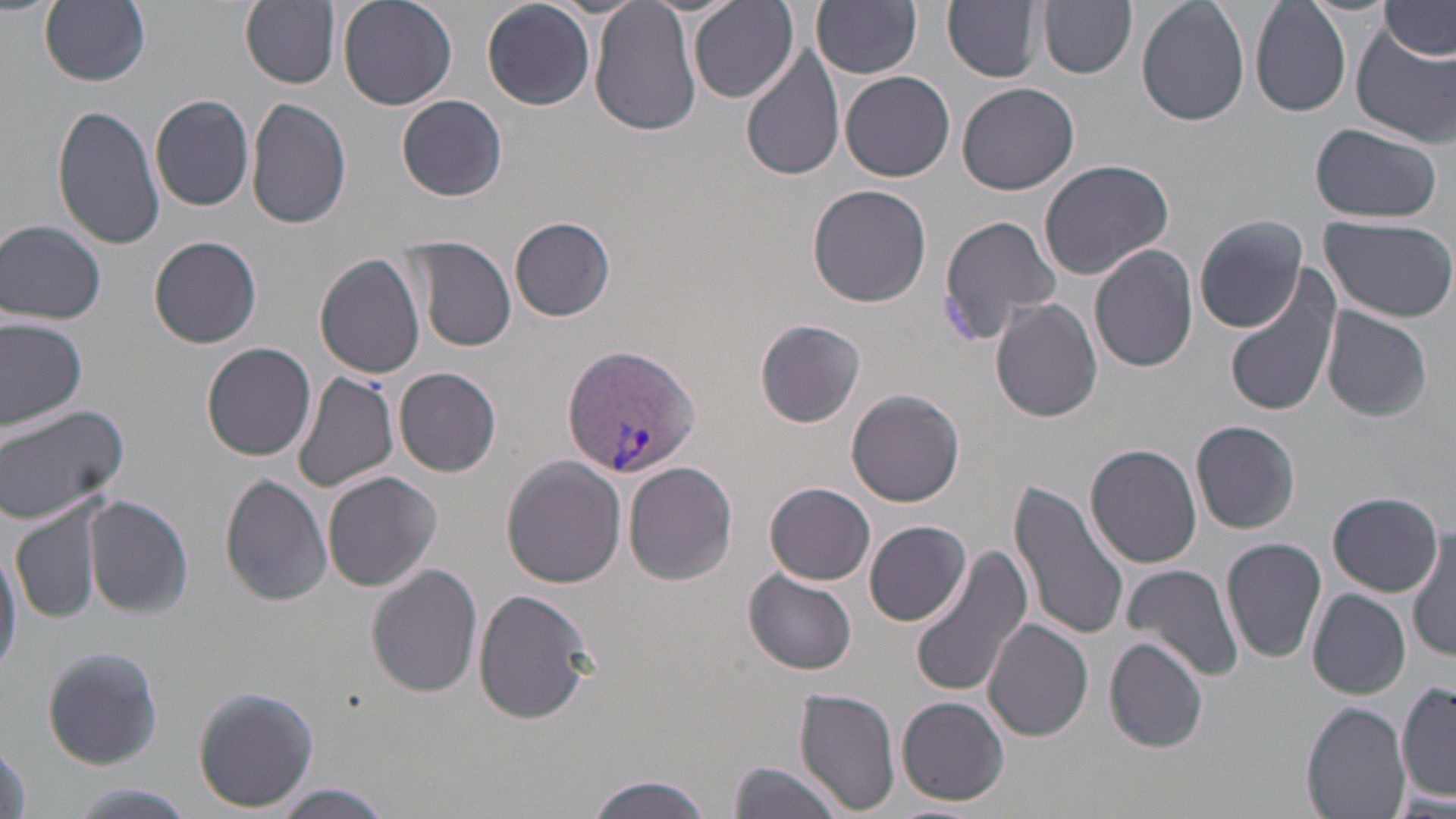

Summary:
  - Coordinate format: approximate bounding boxes as (x1, y1, x2, y2) in pixels
  - Plasmodium vivax-infected red blood cell locations: (563, 344, 700, 477)
  - Uninfected red blood cell locations: (237, 0, 342, 89), (337, 0, 457, 112), (944, 0, 1045, 83), (1040, 0, 1137, 78), (1137, 0, 1251, 126), (1378, 0, 1455, 61), (40, 1, 151, 88), (482, 1, 596, 110), (589, 1, 702, 137), (812, 1, 922, 77), (1250, 1, 1354, 118), (689, 2, 799, 104), (1352, 24, 1455, 146), (739, 46, 847, 180), (841, 71, 955, 181), (958, 82, 1079, 196), (397, 94, 509, 201), (151, 96, 255, 212), (245, 98, 352, 230), (52, 102, 167, 252), (1310, 123, 1443, 224), (1038, 157, 1174, 282), (808, 184, 932, 307), (940, 214, 1062, 342), (1194, 215, 1309, 332), (510, 216, 615, 321), (1320, 216, 1456, 324), (1, 219, 107, 325), (150, 236, 262, 347), (412, 238, 516, 351), (1089, 244, 1197, 373), (314, 253, 427, 379), (1224, 268, 1342, 419), (990, 298, 1103, 422), (1321, 305, 1433, 422), (0, 316, 88, 430), (759, 319, 867, 425), (201, 343, 318, 460), (393, 367, 503, 475), (292, 370, 401, 495), (848, 388, 964, 506), (0, 404, 129, 527), (1189, 419, 1301, 534), (1085, 443, 1202, 570), (502, 457, 627, 588), (624, 461, 738, 586), (324, 470, 442, 592), (220, 473, 333, 607), (1008, 478, 1130, 644), (766, 482, 875, 585), (1326, 492, 1442, 596), (85, 496, 193, 618), (10, 504, 103, 623), (865, 520, 972, 627), (1410, 526, 1456, 663), (1221, 537, 1328, 664), (0, 539, 23, 678), (910, 545, 1034, 699), (1122, 562, 1243, 683), (367, 564, 483, 697), (743, 569, 856, 676), (473, 588, 593, 724), (1307, 589, 1410, 698), (984, 619, 1093, 741), (1104, 635, 1210, 753), (42, 646, 163, 769), (1398, 682, 1456, 801), (191, 686, 318, 811), (794, 687, 900, 816), (897, 695, 1010, 805), (1302, 702, 1410, 819), (0, 737, 31, 819), (726, 761, 844, 819), (585, 775, 714, 819), (265, 785, 398, 818)
  - Slide-level diagnosis: Plasmodium vivax
  - Stain: May-Grünwald-Giemsa
  - Magnification: 1000x
  - Modality: optical microscopy
  - Image size: 1456×819 pixels
  - Field of view: single
  - Preparation: thin blood smear